Assess this cell for malaria.
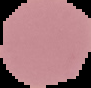
It is uninfected.

Summary:
  - Image size: 91×88 pixels
  - Image type: segmented cell region on a black background
  - Preparation: thin blood smear